State which parasite is depicted.
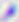
Toxoplasma gondii.

magnification: 400x
modality: micrograph